Report the malaria status of this cell.
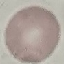

Uninfected.

preparation = thin blood film
image type = automatically extracted cell patch, resized to 64 × 64 pixels
capture = smartphone through the microscope eyepiece
stain = Giemsa